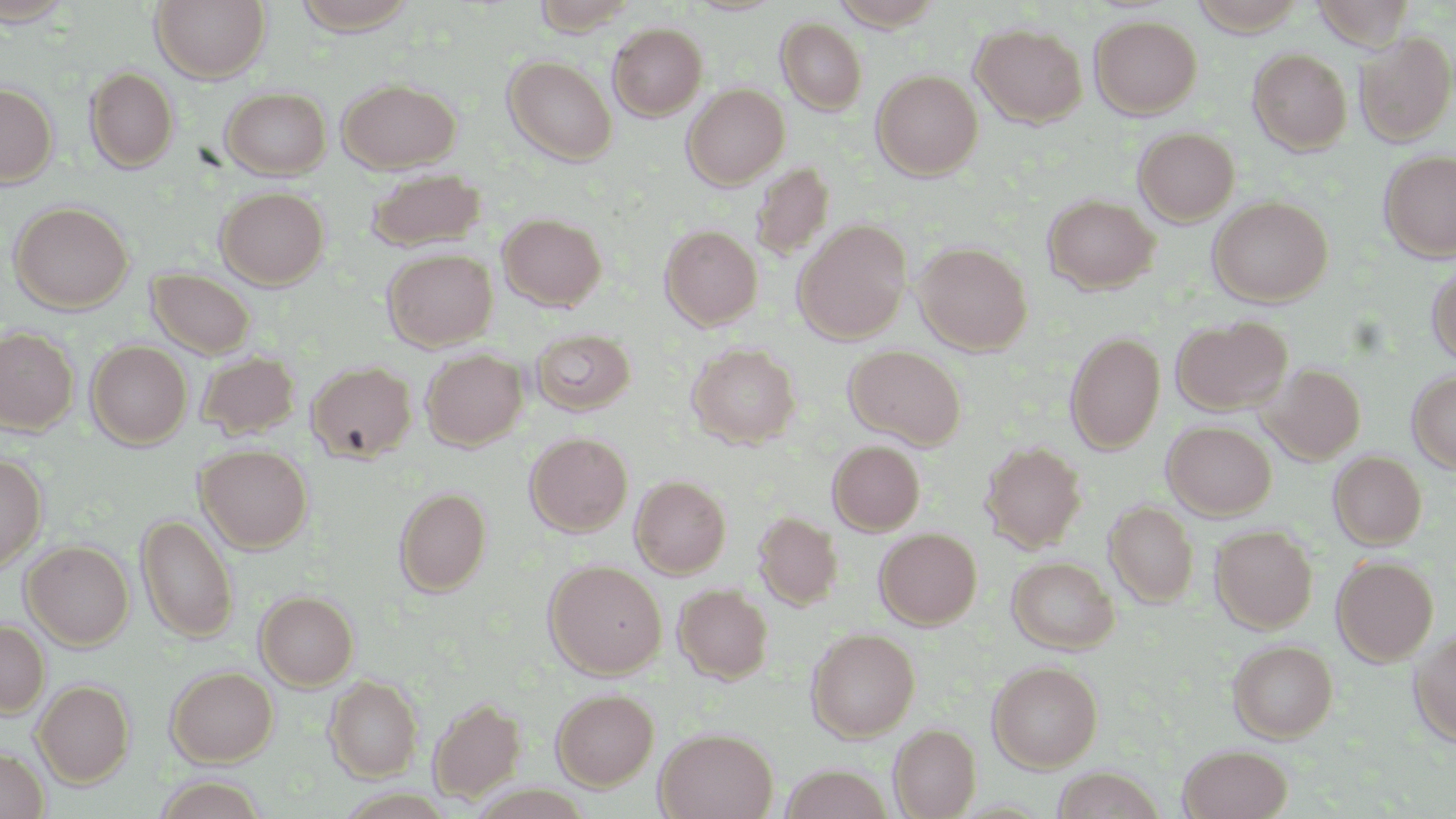
Summary:
  - Coordinate format: approximate bounding boxes as (x1, y1, x2, y2) in pixels
  - Uninfected red blood cell locations: (151, 0, 270, 83), (531, 0, 637, 35), (833, 0, 940, 30), (1190, 0, 1308, 36), (0, 1, 79, 28), (289, 1, 421, 33), (1307, 1, 1420, 49), (1089, 16, 1202, 118), (776, 17, 868, 115), (608, 23, 707, 120), (970, 23, 1087, 127), (1355, 31, 1455, 145), (1248, 48, 1352, 154), (503, 55, 617, 164), (85, 67, 179, 172), (872, 70, 982, 180), (337, 79, 461, 173), (0, 83, 58, 186), (682, 84, 790, 189), (220, 86, 331, 179), (1133, 127, 1240, 225), (1378, 149, 1456, 262), (750, 161, 835, 262), (366, 168, 486, 251), (216, 186, 329, 289), (1043, 194, 1159, 294), (1208, 197, 1333, 306), (9, 201, 133, 314), (498, 212, 607, 311), (793, 220, 911, 343), (660, 225, 762, 329), (914, 241, 1032, 355), (383, 248, 497, 352), (1427, 260, 1456, 367), (147, 268, 255, 358), (1172, 316, 1291, 414), (0, 327, 78, 434), (530, 327, 636, 416), (1065, 332, 1166, 454), (86, 341, 192, 448), (687, 343, 801, 447), (844, 344, 966, 449), (420, 349, 527, 450), (196, 351, 300, 440), (307, 361, 417, 463), (1261, 363, 1366, 465), (1407, 369, 1456, 474), (1162, 421, 1276, 519), (525, 432, 633, 537), (828, 440, 925, 535), (981, 442, 1087, 552), (196, 445, 313, 553), (1329, 451, 1427, 549), (0, 453, 46, 574), (630, 475, 731, 578), (394, 487, 491, 595), (1104, 500, 1199, 607), (752, 511, 843, 610), (136, 514, 238, 643), (1210, 524, 1317, 633), (875, 528, 982, 629), (22, 540, 134, 649), (1332, 555, 1438, 666), (1008, 556, 1119, 653), (545, 560, 666, 678), (674, 583, 773, 683), (255, 591, 359, 690), (0, 620, 49, 717), (806, 628, 920, 741), (1409, 629, 1456, 746), (1228, 639, 1338, 742), (987, 661, 1103, 772), (166, 665, 278, 766), (325, 676, 423, 781), (33, 679, 135, 786), (551, 689, 659, 790), (429, 697, 525, 802), (889, 723, 981, 818), (655, 727, 778, 819), (1178, 744, 1293, 819), (0, 748, 48, 819), (780, 765, 893, 819), (1050, 767, 1166, 819)
  - Slide-level diagnosis: no evidence of blood parasites
  - Stain: May-Grünwald-Giemsa
  - Magnification: 1000x
  - Preparation: thin blood film
  - Image size: 1456×819 pixels
  - Field of view: single
  - Modality: optical microscopy